Identify the parasite.
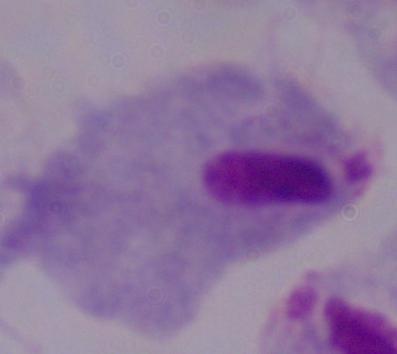

This is a trichomonad.

1000x magnification. Micrograph.